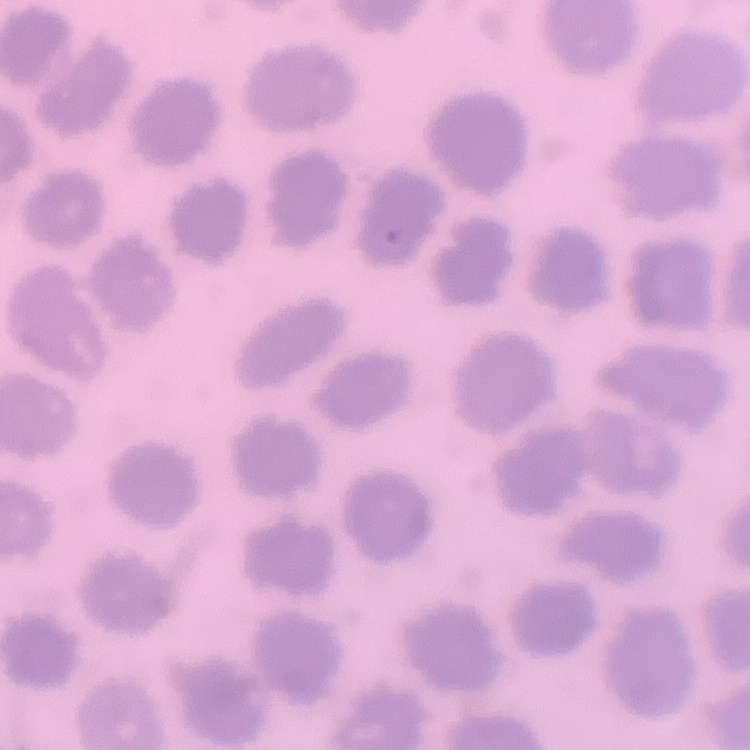

Summary:
  - Erythrocyte morphology: no rouleaux formation
  - Preparation: thin blood smear
  - Image type: one tile cut from a larger photomicrograph
  - Stain: Field's or Giemsa